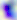
modality = photomicrograph
identification = Toxoplasma gondii
magnification = 400x